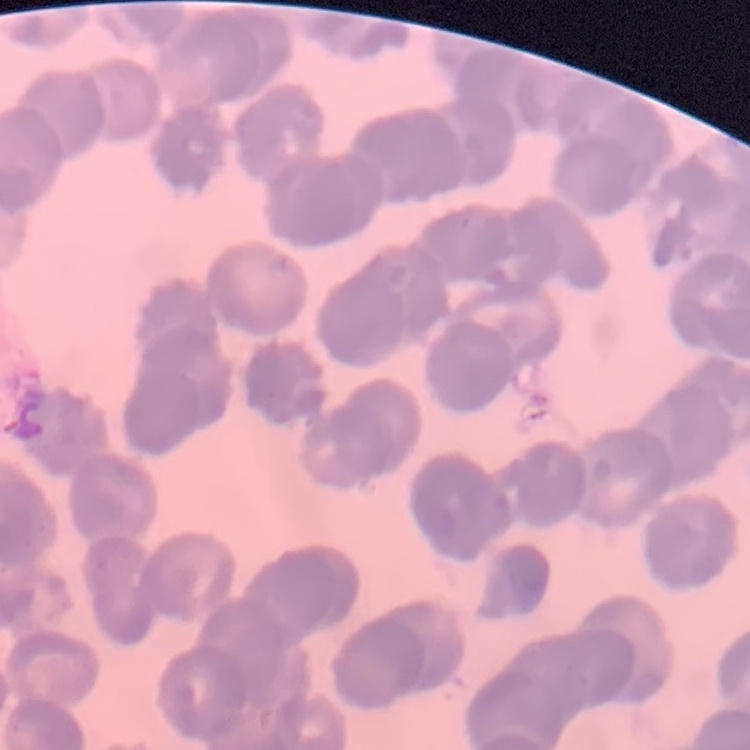
red blood cell morphology = rouleaux formation
preparation = thin blood film
stain = Field's or Giemsa
image type = one tile cut from a larger photomicrograph